Identify the cell.
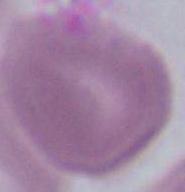
An erythrocyte.

Summary:
  - Modality: micrograph
  - Magnification: 1000x